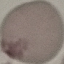
malaria status = uninfected
image type = automatically extracted cell patch, resized to 64 × 64 pixels
stain = Giemsa
capture = smartphone camera at the microscope eyepiece
preparation = thin smear